Assess the morphology of the red blood cells.
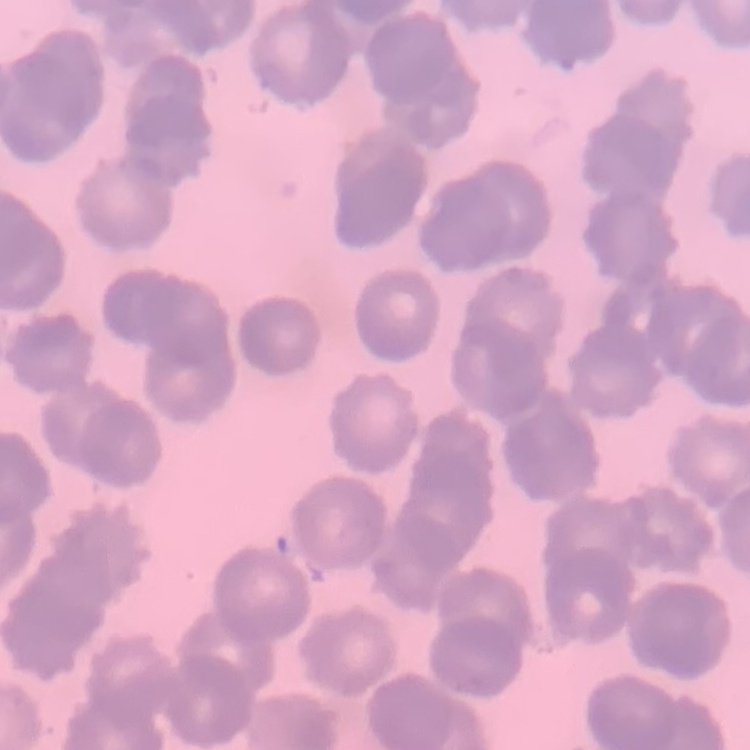

Rouleaux formation.

Field's or Giemsa stain. Square crop of a larger photomicrograph. Thin peripheral smear.